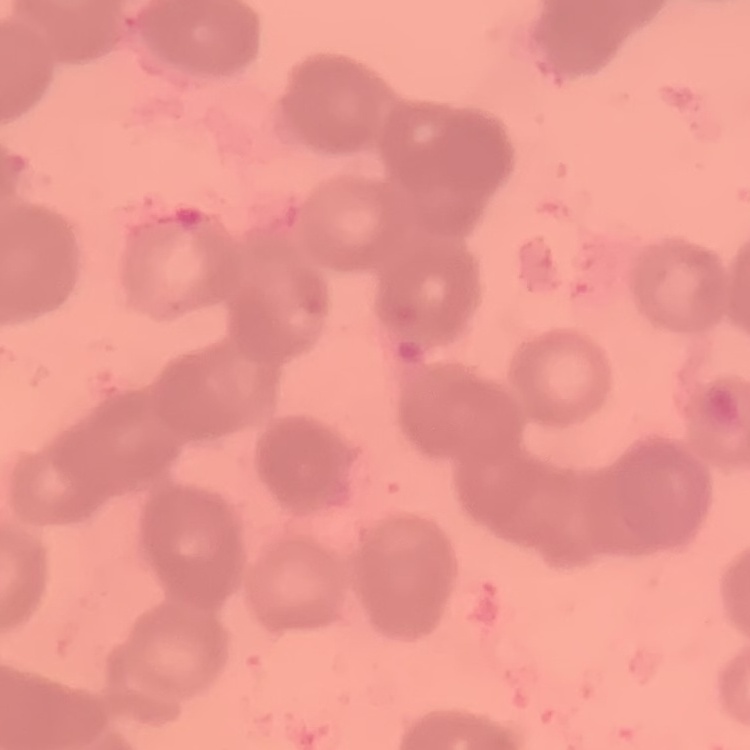

Summary:
  - Red blood cell morphology: rouleaux formation
  - Preparation: thin blood film
  - Image type: square crop of a larger photomicrograph
  - Stain: Field's or Giemsa